Report the malaria status of this cell.
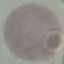

It is uninfected.

Thin blood film. Automatically extracted cell patch, resized to 64 × 64 pixels. Acquired by smartphone through the microscope eyepiece. Giemsa-stained preparation.